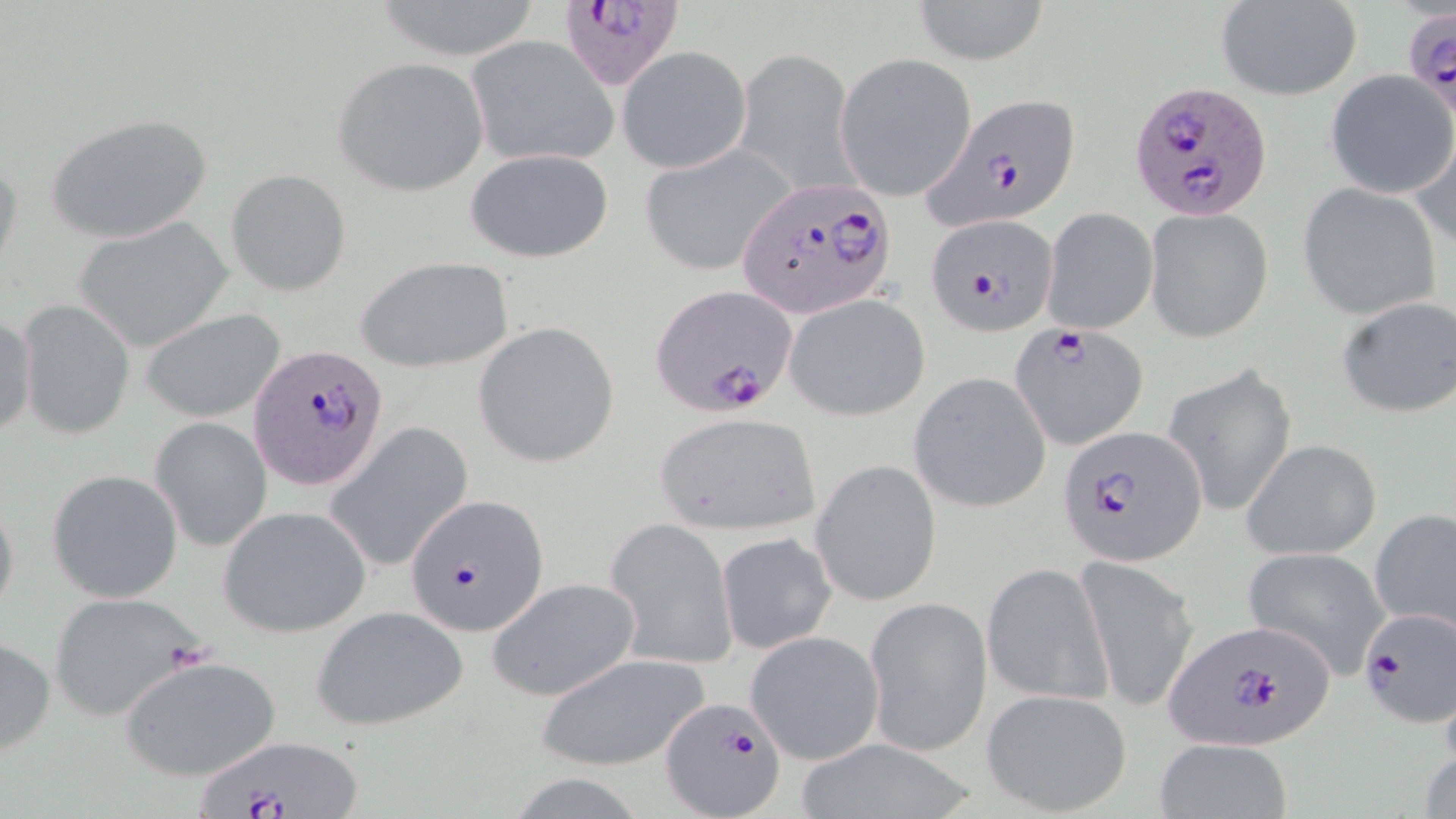

Summary:
  - Coordinate format: approximate bounding boxes as [x1, y1, x2, y2] in pixels
  - Plasmodium falciparum-infected red blood cell locations: [553, 1, 688, 92], [1406, 12, 1455, 123], [1127, 77, 1274, 218], [923, 92, 1081, 227], [738, 178, 894, 320], [925, 213, 1060, 335], [652, 285, 798, 416], [1012, 323, 1145, 447], [249, 344, 390, 493], [1059, 421, 1207, 565], [407, 494, 550, 637], [1354, 604, 1455, 728], [1164, 619, 1337, 750], [662, 696, 787, 818], [196, 737, 366, 819]
  - Uninfected red blood cell locations: [369, 0, 547, 62], [912, 0, 1050, 65], [1214, 2, 1362, 100], [466, 35, 620, 169], [617, 46, 752, 174], [733, 48, 860, 196], [835, 54, 978, 200], [333, 57, 489, 197], [1325, 71, 1455, 196], [48, 112, 213, 246], [1407, 132, 1456, 251], [638, 143, 798, 276], [0, 146, 22, 279], [464, 147, 614, 264], [226, 169, 351, 296], [1298, 182, 1440, 320], [1041, 208, 1158, 335], [1145, 208, 1273, 343], [72, 218, 234, 352], [356, 255, 516, 373], [786, 294, 929, 419], [1336, 294, 1456, 418], [17, 299, 135, 439], [138, 307, 287, 424], [1, 311, 37, 440], [473, 321, 621, 467], [1165, 363, 1298, 517], [910, 372, 1051, 512], [653, 410, 823, 534], [151, 417, 273, 552], [324, 422, 474, 574], [1241, 438, 1382, 561], [811, 459, 942, 607], [47, 470, 183, 603], [0, 490, 20, 629], [219, 505, 372, 638], [1370, 506, 1456, 637], [605, 517, 736, 671], [717, 532, 837, 653], [1243, 547, 1391, 680], [1074, 555, 1200, 713], [981, 562, 1115, 708], [487, 577, 642, 701], [48, 592, 207, 722], [864, 596, 991, 757], [309, 605, 470, 732], [744, 630, 884, 764], [0, 635, 55, 758], [535, 650, 710, 772], [119, 655, 281, 781], [981, 688, 1134, 817], [1154, 737, 1293, 819], [789, 738, 983, 819]
  - Slide-level diagnosis: Plasmodium falciparum
  - Preparation: thin blood smear
  - Magnification: 1000x
  - Field of view: single
  - Image size: 1456×819 pixels
  - Modality: optical microscopy
  - Stain: May-Grünwald-Giemsa